Outline each uninfected red blood cell.
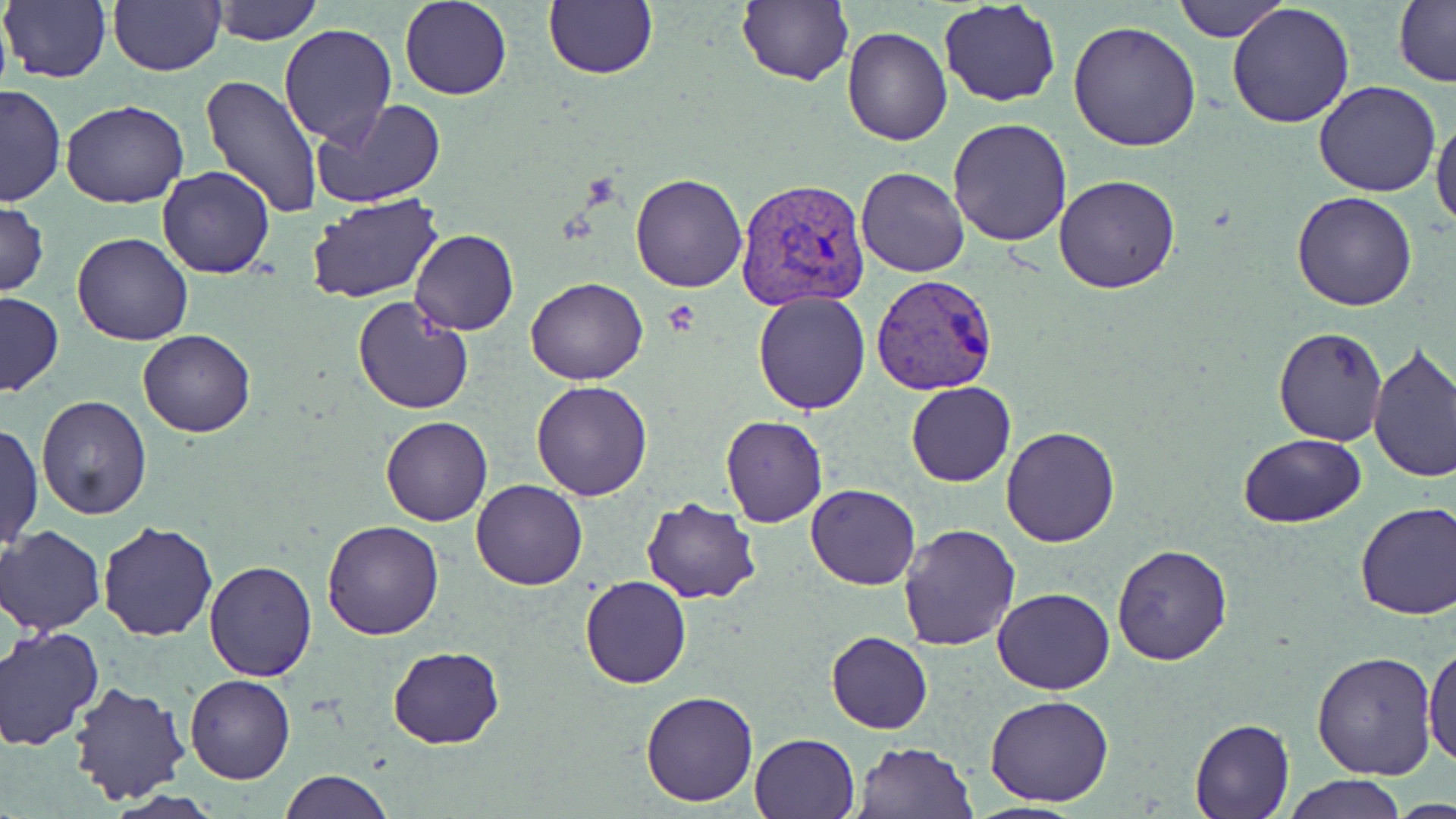
Approximate bounding boxes as (x1, y1, x2, y2) in pixels.
Uninfected red blood cells: (210, 0, 323, 45), (399, 0, 513, 100), (737, 0, 853, 85), (1173, 0, 1291, 42), (1, 1, 112, 83), (108, 1, 226, 75), (542, 1, 659, 80), (938, 1, 1061, 107), (1227, 2, 1356, 130), (1392, 2, 1456, 84), (1068, 22, 1202, 153), (279, 24, 397, 148), (841, 27, 952, 147), (203, 76, 323, 219), (1313, 81, 1442, 198), (0, 84, 64, 207), (310, 99, 446, 209), (60, 100, 188, 208), (1431, 109, 1456, 232), (948, 117, 1073, 246), (156, 166, 275, 279), (857, 167, 970, 277), (629, 172, 748, 292), (1054, 175, 1180, 293), (1292, 192, 1418, 311), (307, 195, 444, 304), (0, 198, 47, 298), (410, 229, 519, 335), (71, 231, 195, 346), (525, 277, 649, 385), (753, 290, 871, 413), (1, 291, 63, 397), (352, 296, 473, 414), (1272, 326, 1389, 447), (139, 328, 255, 437), (1367, 343, 1456, 485), (531, 379, 653, 501), (906, 380, 1015, 488), (35, 394, 154, 520), (720, 415, 828, 528), (380, 416, 492, 526), (1, 422, 43, 551), (1001, 428, 1119, 548), (1238, 433, 1366, 526), (471, 478, 587, 591), (805, 483, 919, 591), (641, 498, 761, 602), (1354, 500, 1456, 618), (322, 519, 446, 640), (98, 522, 217, 642), (897, 523, 1020, 650), (2, 525, 106, 635), (1110, 544, 1233, 665), (204, 558, 317, 680), (579, 575, 692, 689), (991, 588, 1115, 695), (1, 627, 105, 750), (825, 631, 932, 734), (1423, 644, 1456, 767), (387, 645, 506, 748), (1312, 648, 1440, 779), (185, 675, 296, 785), (67, 682, 192, 805), (640, 690, 759, 807), (985, 694, 1116, 806), (1190, 717, 1295, 819), (750, 733, 860, 819), (851, 739, 979, 819), (281, 770, 391, 819), (1282, 775, 1406, 817).

Platelet locations: (663, 298, 701, 336). Plasmodium vivax-infected red blood cell locations: (734, 174, 872, 310), (870, 272, 998, 396). Slide-level diagnosis: Plasmodium vivax. One field of a larger specimen. Image is 1456×819 pixels. 1000x magnification. Thin blood smear. Optical microscopy. May-Grünwald-Giemsa stain.